Report the malaria status of this cell.
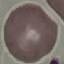
It is uninfected.

Summary:
  - Preparation: thin blood film
  - Stain: Giemsa
  - Capture: smartphone camera at the microscope eyepiece
  - Image type: automatically extracted cell patch, resized to 64 × 64 pixels